Name the parasite shown.
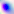

This is Toxoplasma gondii.

Micrograph. Captured at 400x magnification.